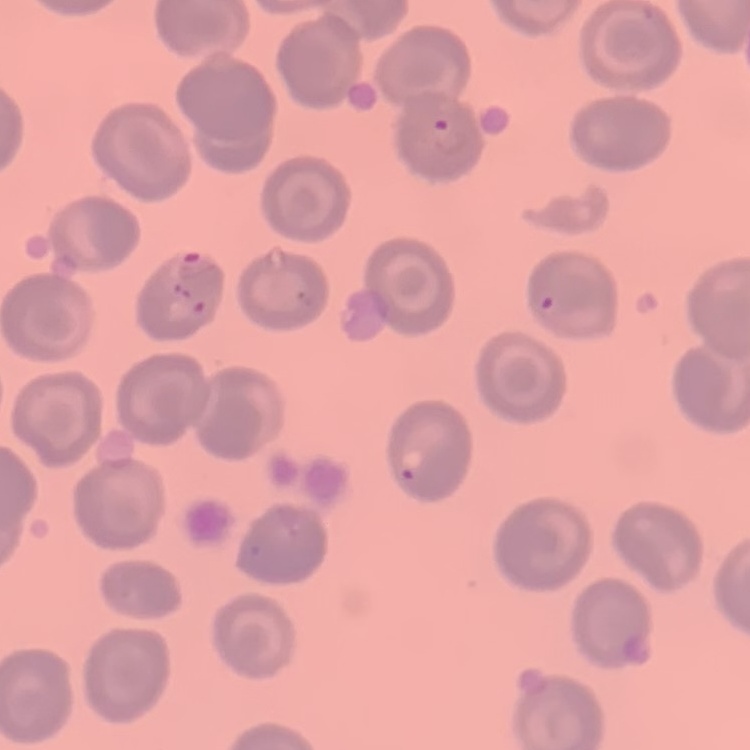
The erythrocytes exhibit no rouleaux formation. Field's or Giemsa stain. Thin blood smear. One tile cut from a larger photomicrograph.